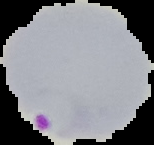
Image is 154×145 pixels. Malaria status: parasitized. From a thin blood smear. Cell region segmented out of the field of view; the surrounding area is masked to black.